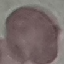

result = negative for malaria parasites
preparation = thin blood film
stain = Giemsa
image type = cell patch, automatically extracted from a larger field of view and resized to 64 × 64 pixels
capture = smartphone through the microscope eyepiece